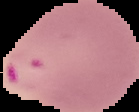
Summary:
  - Preparation: thin blood smear
  - Image size: 139×112 pixels
  - Image type: segmented cell region with the area outside set to black
  - Result: malaria parasites detected